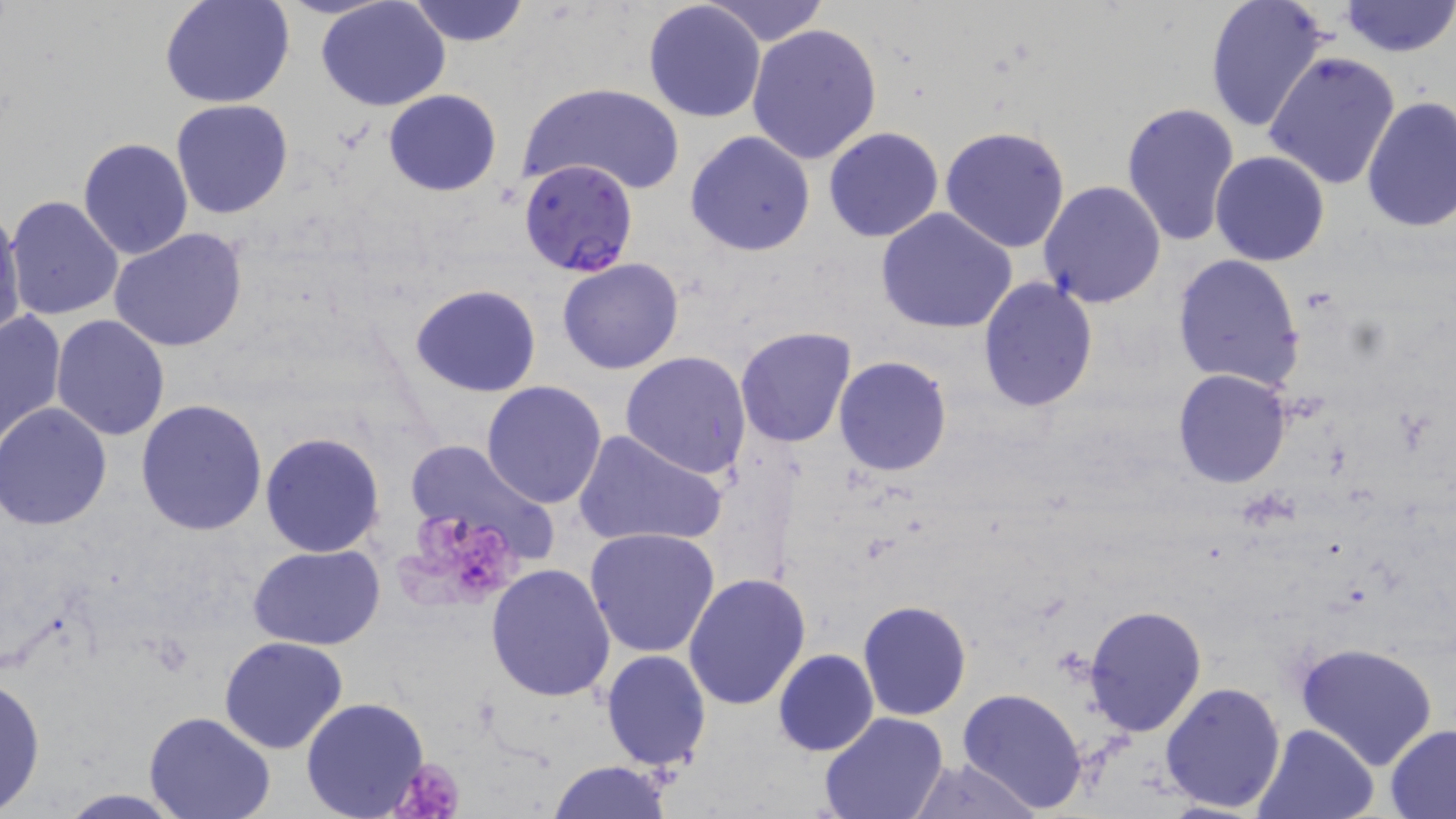
Summary:
  - Coordinate format: approximate bounding boxes as (x1, y1, x2, y2) in pixels
  - Platelet locations: (391, 508, 528, 615), (390, 756, 468, 819)
  - Uninfected red blood cell locations: (160, 0, 295, 108), (318, 0, 450, 111), (407, 0, 529, 47), (706, 0, 829, 44), (1202, 0, 1333, 136), (1339, 0, 1454, 57), (642, 1, 766, 122), (745, 21, 884, 163), (1264, 52, 1401, 189), (520, 82, 686, 197), (384, 88, 503, 195), (1360, 97, 1456, 233), (170, 99, 294, 220), (1121, 101, 1241, 247), (939, 125, 1072, 251), (823, 126, 944, 242), (684, 129, 815, 258), (78, 137, 192, 259), (1210, 150, 1330, 266), (1038, 179, 1166, 307), (6, 195, 124, 321), (0, 206, 26, 344), (875, 207, 1021, 335), (109, 229, 248, 353), (1171, 254, 1305, 390), (556, 257, 685, 375), (977, 276, 1101, 413), (408, 283, 543, 398), (0, 309, 67, 450), (50, 314, 171, 440), (733, 326, 858, 448), (620, 352, 752, 479), (833, 355, 954, 476), (1172, 368, 1292, 489), (480, 380, 608, 510), (136, 398, 269, 537), (0, 403, 112, 530), (572, 427, 728, 550), (259, 431, 385, 558), (406, 438, 559, 569), (585, 528, 720, 659), (247, 545, 387, 651), (485, 563, 617, 703), (683, 571, 813, 709), (860, 599, 971, 719), (1083, 604, 1209, 738), (219, 635, 347, 755), (1294, 641, 1439, 770), (773, 649, 878, 758), (602, 650, 712, 771), (0, 673, 46, 814), (1160, 681, 1288, 813), (957, 687, 1090, 815), (300, 697, 429, 819), (818, 710, 949, 819), (143, 712, 276, 819), (1254, 722, 1381, 819), (1384, 723, 1456, 817), (904, 759, 1042, 817), (547, 760, 674, 818), (53, 790, 187, 818)
  - Plasmodium falciparum-infected red blood cell locations: (518, 158, 638, 277)
  - Slide-level diagnosis: Plasmodium falciparum
  - Preparation: thin blood film
  - Modality: optical microscopy
  - Field of view: one of a larger specimen
  - Image size: 1456×819 pixels
  - Stain: May-Grünwald-Giemsa
  - Magnification: 1000x